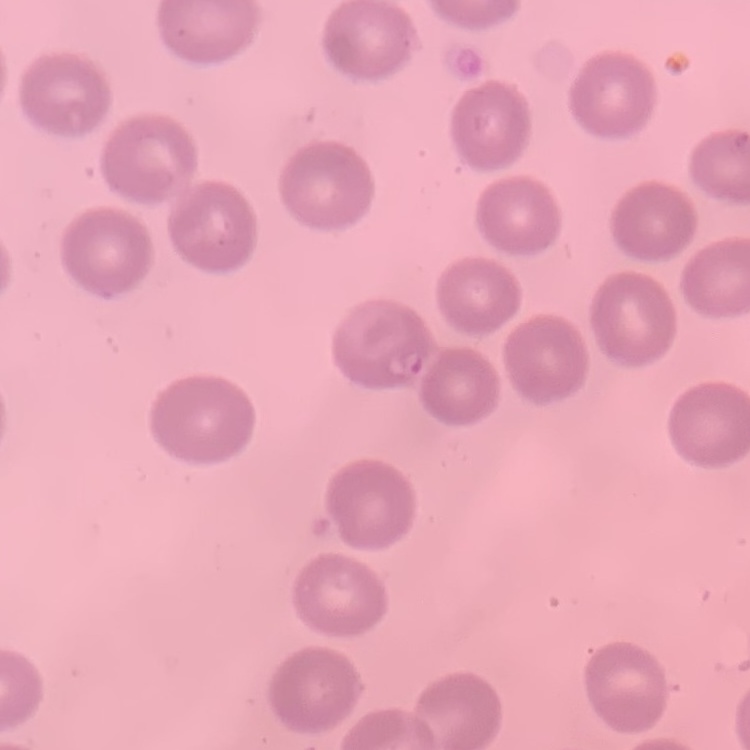 The erythrocytes show no rouleaux formation. Stained with either Field's or Giemsa. One tile cut from a larger photomicrograph. Thin blood smear.